Point out each Plasmodium parasite.
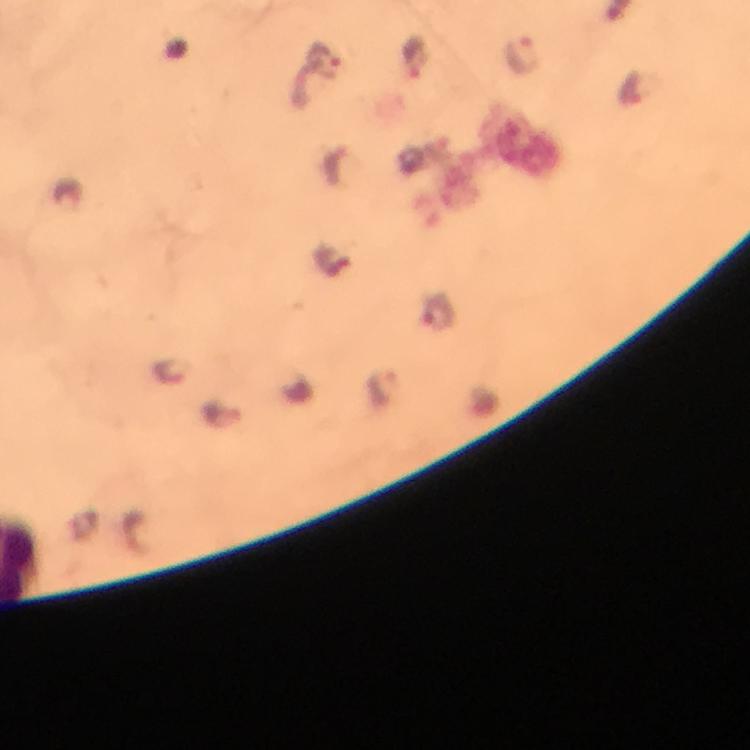

Approximate centers as [x, y] in pixels.
Plasmodium parasites: [522, 52], [418, 55], [325, 58], [438, 311], [170, 370], [382, 387].

From a malaria diagnostic workup. 100x magnification. Giemsa-stained preparation. Cropped region of a single field of view. Photographed with a smartphone mounted on the microscope. Thick smear. Immersion oil was used. Image is 750×750 pixels.